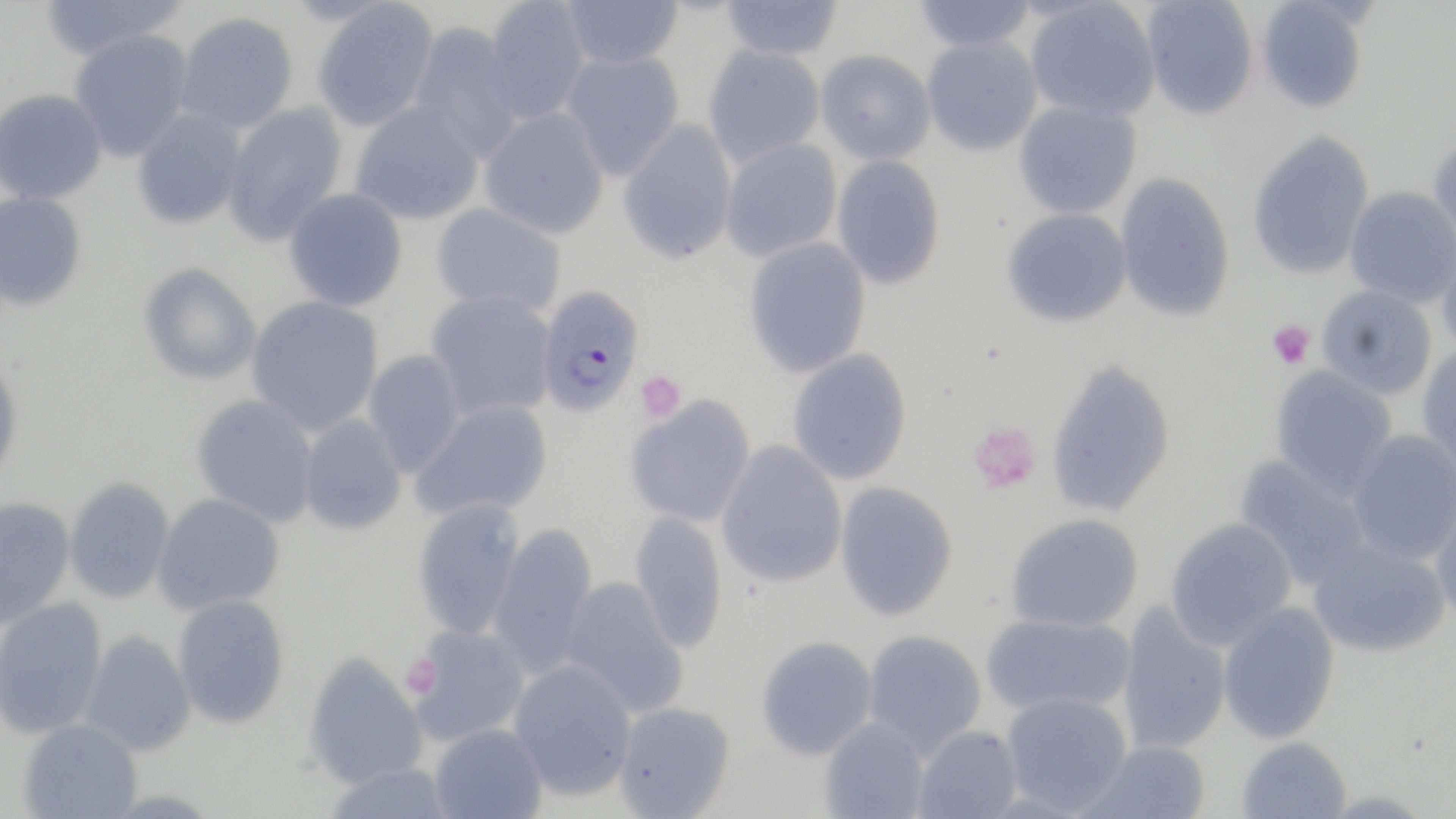
Summary:
  - Coordinate format: approximate bounding boxes as [x1, y1, x2, y2] in pixels
  - Platelet locations: [1267, 320, 1315, 370], [635, 371, 687, 423], [967, 421, 1041, 494]
  - Uninfected red blood cell locations: [37, 0, 189, 61], [480, 0, 589, 124], [559, 0, 683, 70], [717, 0, 844, 61], [911, 0, 1039, 53], [1024, 0, 1160, 121], [1140, 0, 1259, 120], [1254, 0, 1369, 114], [311, 1, 440, 132], [174, 12, 298, 134], [408, 23, 522, 159], [69, 29, 193, 161], [920, 35, 1043, 155], [701, 43, 826, 168], [559, 49, 685, 179], [815, 49, 935, 164], [0, 89, 108, 205], [1013, 100, 1142, 220], [349, 101, 485, 225], [222, 102, 348, 246], [479, 107, 610, 239], [131, 108, 246, 229], [617, 120, 738, 264], [1247, 130, 1375, 280], [1427, 134, 1456, 259], [719, 138, 842, 262], [831, 153, 946, 291], [1114, 172, 1235, 322], [1344, 187, 1455, 308], [283, 188, 408, 312], [0, 191, 88, 311], [431, 203, 567, 316], [1001, 207, 1132, 327], [742, 237, 871, 378], [1437, 243, 1456, 362], [138, 263, 262, 386], [1315, 285, 1438, 399], [425, 290, 556, 421], [246, 295, 384, 436], [1416, 346, 1456, 478], [786, 348, 912, 485], [362, 350, 467, 477], [1045, 357, 1177, 519], [0, 359, 23, 486], [1269, 365, 1398, 500], [190, 393, 320, 527], [625, 395, 756, 528], [410, 399, 553, 522], [298, 414, 406, 536], [1346, 429, 1456, 565], [715, 441, 848, 589], [1233, 454, 1372, 590], [64, 477, 176, 604], [834, 481, 958, 621], [1429, 491, 1456, 631], [152, 493, 285, 614], [0, 497, 76, 629], [412, 498, 526, 639], [629, 508, 729, 654], [1005, 513, 1144, 633], [1164, 517, 1297, 650], [487, 524, 599, 677], [1307, 536, 1451, 658], [558, 576, 687, 717], [172, 594, 290, 729], [0, 597, 108, 739], [1217, 601, 1341, 743], [1115, 603, 1233, 755], [980, 612, 1135, 717], [406, 624, 531, 746], [78, 629, 197, 756], [862, 629, 987, 757], [756, 635, 878, 760], [303, 651, 428, 789], [507, 658, 638, 801], [1000, 691, 1133, 815], [611, 701, 736, 819], [819, 716, 930, 818], [17, 718, 142, 818], [429, 722, 547, 819], [912, 724, 1023, 819], [1235, 736, 1351, 818], [1077, 739, 1212, 818]
  - Plasmodium falciparum-infected red blood cell locations: [535, 284, 645, 418]
  - Slide-level diagnosis: Plasmodium falciparum
  - Stain: May-Grünwald-Giemsa
  - Modality: optical microscopy
  - Preparation: thin blood smear
  - Image size: 1456×819 pixels
  - Field of view: one of a larger specimen
  - Magnification: 1000x